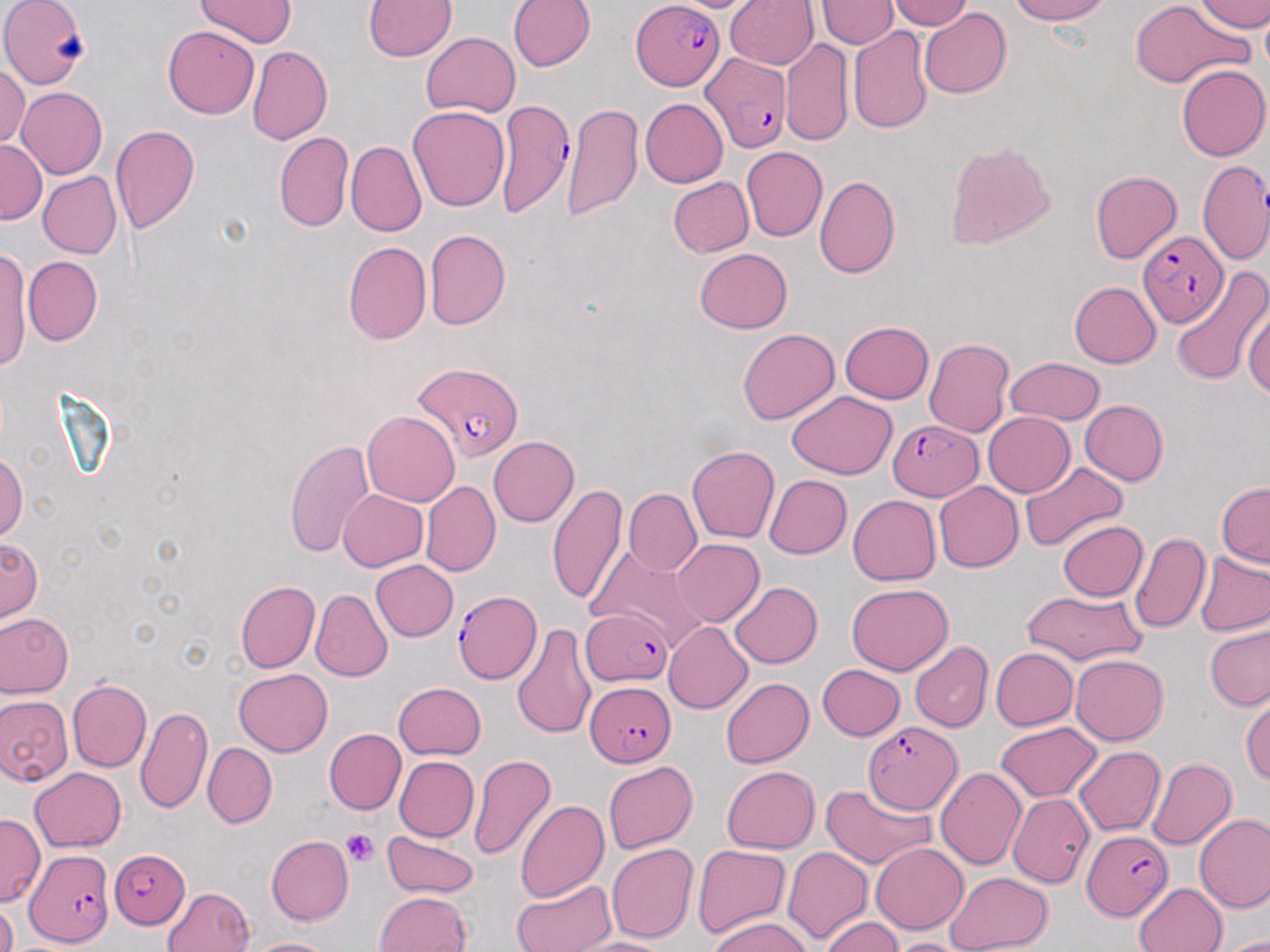

{
  "slide_level_diagnosis": "Plasmodium falciparum",
  "field_of_view": "single",
  "plasmodium_falciparum_infected_red_blood_cell_locations": "approximate bounding boxes as (x1,y1)-(x2,y2) corner pairs in pixels: (632,0)-(724,90), (699,52)-(790,152), (495,99)-(575,220), (1196,158)-(1268,267), (1139,230)-(1225,324), (412,361)-(524,460), (886,420)-(982,500), (453,591)-(539,684), (581,608)-(674,687), (584,680)-(676,764), (863,721)-(963,814), (1085,832)-(1170,920), (26,848)-(115,948), (109,849)-(190,928)",
  "preparation": "thin blood smear",
  "platelet_locations": "approximate bounding boxes as (x1,y1)-(x2,y2) corner pairs in pixels: (340,828)-(380,866)",
  "image_size": "1270×952 pixels",
  "stain": "May-Grünwald-Giemsa",
  "modality": "light microscopy",
  "magnification": "1000x",
  "uninfected_red_blood_cell_locations": "approximate bounding boxes as (x1,y1)-(x2,y2) corner pairs in pixels: (195,0)-(296,49), (363,0)-(456,59), (507,0)-(595,71), (724,0)-(819,68), (1009,0)-(1111,24), (1132,0)-(1245,88), (1194,0)-(1270,33), (1,1)-(89,87), (815,1)-(899,50), (887,1)-(975,30), (919,7)-(1011,99), (1260,10)-(1270,79), (162,25)-(259,118), (847,25)-(934,134), (422,32)-(520,117), (780,39)-(854,145), (247,46)-(332,145), (0,63)-(30,148), (1177,64)-(1270,161), (17,86)-(107,179), (640,99)-(728,187), (561,101)-(643,221), (408,106)-(509,211), (109,124)-(200,235), (273,131)-(353,233), (0,138)-(47,224), (345,140)-(426,237), (945,140)-(1056,249), (741,147)-(827,243), (1090,170)-(1182,264), (38,172)-(122,259), (813,175)-(900,279), (666,176)-(753,258), (424,229)-(510,330), (342,241)-(431,345), (694,247)-(792,334), (0,249)-(32,369), (24,256)-(102,345), (1168,266)-(1270,384), (1068,281)-(1161,368), (1242,298)-(1270,401), (840,320)-(933,403), (738,329)-(839,424), (923,338)-(1016,437), (1005,357)-(1104,425), (788,391)-(897,479), (1079,400)-(1169,485), (362,410)-(459,506), (983,412)-(1075,497), (488,436)-(580,526), (283,438)-(375,559), (687,445)-(779,543), (0,452)-(27,540), (1020,461)-(1128,550), (764,475)-(851,558), (421,480)-(500,576), (934,482)-(1024,573), (1216,482)-(1270,568), (547,483)-(626,605), (623,489)-(701,576), (338,490)-(429,571), (847,495)-(940,585), (1057,519)-(1148,601), (1129,531)-(1211,636), (1,537)-(41,620), (672,539)-(764,627), (586,547)-(707,650), (1194,551)-(1270,636), (371,560)-(459,640), (235,580)-(320,673), (729,581)-(822,669), (846,583)-(952,676), (311,589)-(393,682), (1020,590)-(1146,666), (0,613)-(73,697), (663,621)-(753,713), (511,622)-(596,740), (1205,626)-(1270,710), (909,641)-(993,732), (990,648)-(1078,731), (1071,654)-(1168,745), (818,663)-(905,741), (233,668)-(333,756), (721,678)-(814,768), (67,679)-(152,773), (393,682)-(487,759), (1240,693)-(1269,784), (0,694)-(72,786), (136,706)-(212,814), (997,721)-(1101,802), (324,729)-(406,815), (203,742)-(277,828), (1073,746)-(1165,835), (468,754)-(558,862), (394,755)-(479,842), (1147,757)-(1236,850), (603,761)-(698,853), (721,766)-(820,854), (30,767)-(126,852), (934,767)-(1026,870), (819,782)-(934,869), (1007,795)-(1093,887), (515,799)-(609,902), (1194,813)-(1270,913), (0,814)-(44,905), (381,829)-(479,898), (265,835)-(354,925), (870,842)-(968,933), (606,843)-(699,943), (691,844)-(789,939), (783,847)-(873,943), (944,871)-(1052,952), (511,877)-(616,952), (1134,883)-(1227,952), (163,886)-(254,952), (374,891)-(472,952), (1,901)-(18,952), (710,916)-(814,952), (820,917)-(903,952), (1213,934)-(1270,952), (243,937)-(338,952), (570,937)-(676,952), (890,937)-(974,952)"
}